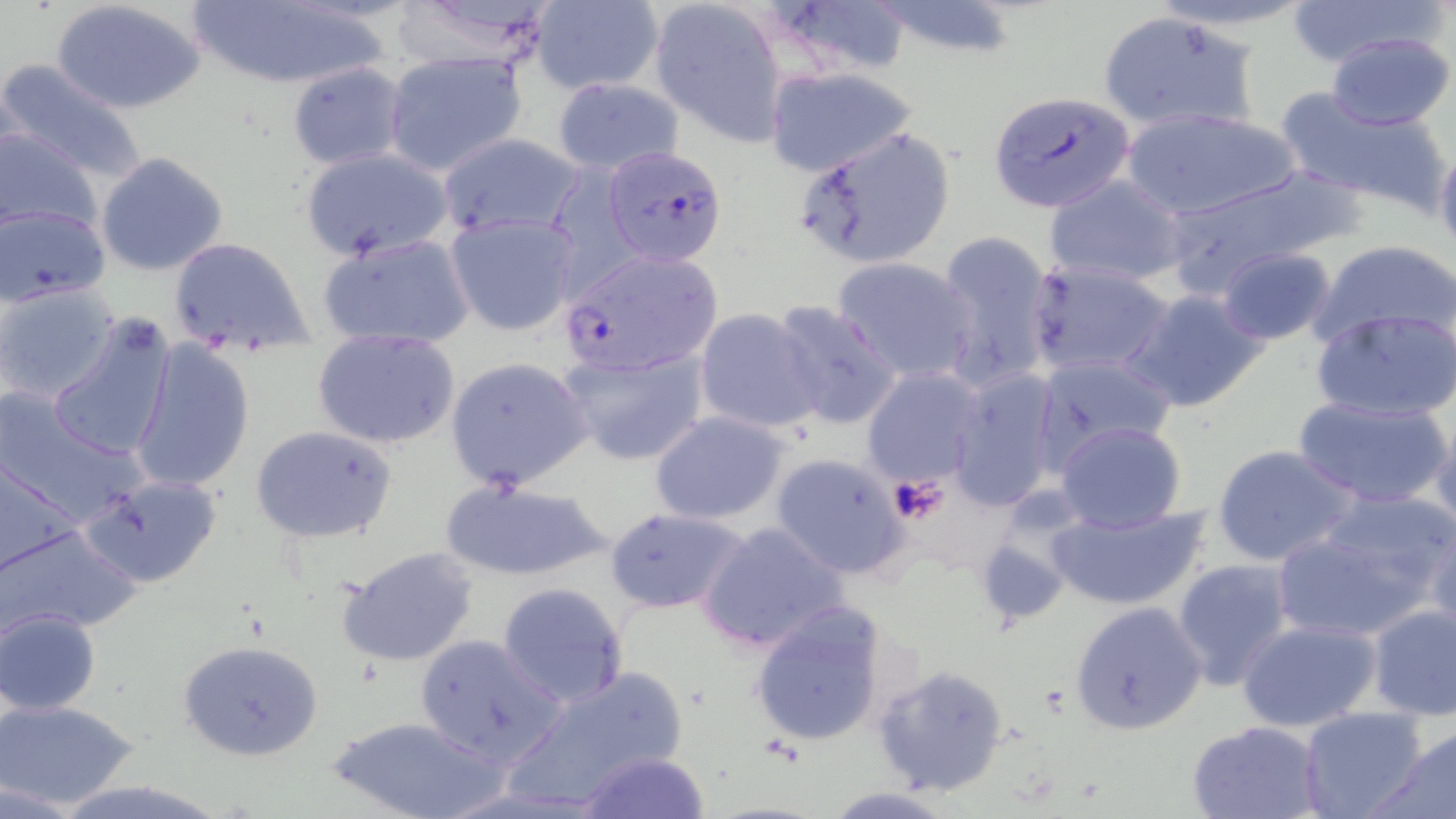

Approximate bounding boxes as (x1,y1)-(x2,y2) corner pairs in pixels. Uninfected red blood cell locations: (53,0)-(206,115), (189,0)-(382,88), (395,0)-(566,68), (649,0)-(787,144), (758,0)-(916,83), (1282,0)-(1441,68), (530,1)-(664,93), (865,1)-(1026,60), (1096,11)-(1258,134), (1325,32)-(1456,130), (381,50)-(529,175), (0,57)-(150,184), (287,62)-(405,168), (766,66)-(920,177), (551,76)-(685,176), (1275,88)-(1449,210), (1118,106)-(1303,221), (793,124)-(956,270), (0,126)-(102,235), (437,132)-(584,236), (1434,146)-(1456,265), (300,147)-(452,263), (96,152)-(229,277), (1157,172)-(1347,299), (1044,173)-(1187,286), (1,203)-(111,305), (444,212)-(579,337), (316,231)-(473,350), (936,232)-(1057,391), (167,236)-(314,357), (1313,238)-(1455,351), (1216,246)-(1338,346), (831,256)-(978,384), (1027,260)-(1174,378), (0,283)-(121,405), (1124,288)-(1269,414), (769,300)-(905,431), (694,307)-(824,435), (1312,307)-(1456,422), (47,314)-(177,461), (313,328)-(462,450), (130,340)-(255,493), (558,347)-(709,466), (1030,354)-(1177,465), (444,356)-(593,492), (861,366)-(987,490), (946,368)-(1064,511), (0,388)-(142,523), (1294,394)-(1450,510), (648,410)-(792,525), (1428,411)-(1456,535), (1053,421)-(1187,533), (249,425)-(398,544), (1211,445)-(1358,568), (769,450)-(907,580), (0,461)-(82,576), (81,472)-(225,589), (439,478)-(611,585), (1045,502)-(1207,612), (604,507)-(748,614), (1273,508)-(1446,642), (1424,519)-(1456,644), (696,520)-(850,655), (0,523)-(140,636), (338,545)-(481,668), (1171,557)-(1296,692), (498,582)-(629,707), (749,600)-(895,750), (1069,601)-(1209,736), (1365,605)-(1456,721), (2,609)-(102,715), (1237,619)-(1383,734), (410,632)-(567,769), (178,638)-(324,761), (870,664)-(1008,798), (507,666)-(688,804), (0,698)-(140,810), (1299,708)-(1429,819), (329,714)-(502,819), (1186,719)-(1328,819), (1374,723)-(1456,819), (575,751)-(708,818), (816,788)-(964,818). Plasmodium falciparum-infected red blood cell locations: (989,91)-(1137,212), (602,145)-(729,266), (557,249)-(727,380). Platelet locations: (888,475)-(951,524). Slide-level diagnosis: Plasmodium falciparum. One field of a larger specimen. Image is 1456×819 pixels. Optical microscopy. Thin blood film. Captured at 1000x magnification. May-Grünwald-Giemsa stain.